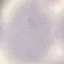

Summary:
  - Malaria status: uninfected
  - Preparation: thin blood smear
  - Image type: automatically extracted cell patch, resized to 64 × 64 pixels
  - Stain: Giemsa
  - Capture: smartphone through the microscope eyepiece